Classify this cell by malaria status.
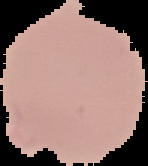

Uninfected.

image size = 148×166 pixels
image type = segmented cell region with the area outside set to black
preparation = thin blood smear